Classify this cell by malaria status.
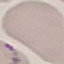
It is uninfected.

Thin smear of blood. Giemsa stain. Photographed with a smartphone camera at the microscope eyepiece. Automatically extracted cell patch, resized to 64 × 64 pixels.